Classify this cell by malaria status.
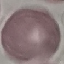

It is uninfected.

Summary:
  - Capture: smartphone through the microscope eyepiece
  - Preparation: thin smear
  - Stain: Giemsa
  - Image type: cell patch, automatically extracted from a larger field of view and resized to 64 × 64 pixels